Point out each leukocyte.
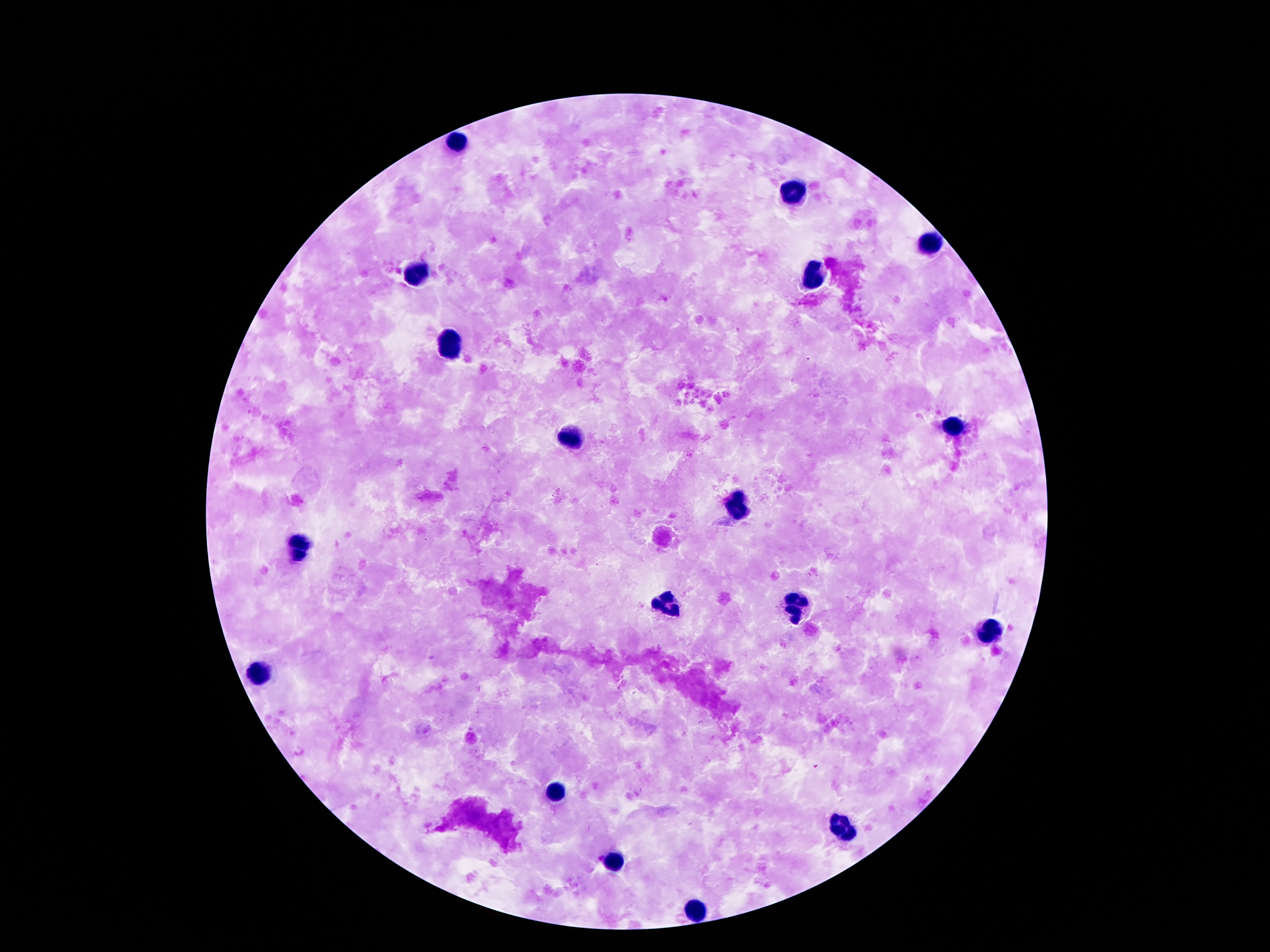
Approximate centers as {x, y} in pixels.
Leukocytes: {458, 142}, {796, 190}, {931, 242}, {815, 271}, {418, 274}, {448, 344}, {954, 426}, {566, 435}, {734, 508}, {305, 546}, {670, 601}, {798, 604}, {990, 630}, {259, 669}, {557, 794}, {840, 829}, {612, 861}, {694, 909}.

One field from this slide. Giemsa-stained preparation. Patient malaria status: not infected. Image is 1270×952 pixels. 100x magnification. Photographed through the microscope eyepiece with a smartphone camera. Thick blood film.